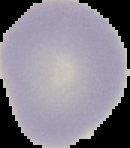
Summary:
  - Result: negative for Plasmodium parasites
  - Preparation: thin blood film
  - Image size: 130×148 pixels
  - Image type: cell region segmented out of the field of view; surrounding area masked to black